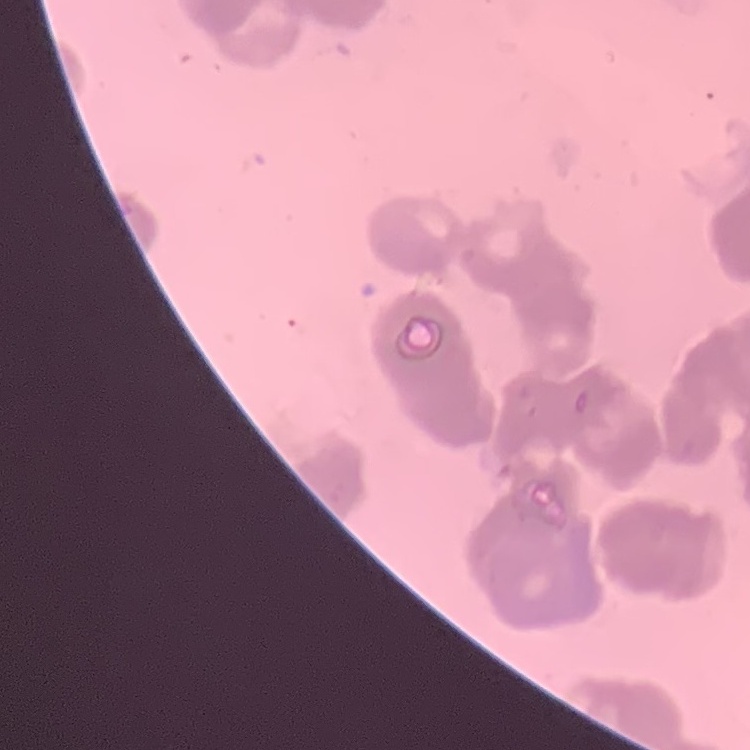

The erythrocytes show rouleaux formation. Thin blood smear. Square crop of a larger photomicrograph. Field's or Giemsa stain.